Classify this cell by malaria status.
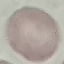
It is uninfected.

Acquired by smartphone through the microscope eyepiece. Thin smear of blood. Cell patch, automatically extracted from a larger field of view and resized to 64 × 64 pixels. Giemsa-stained preparation.